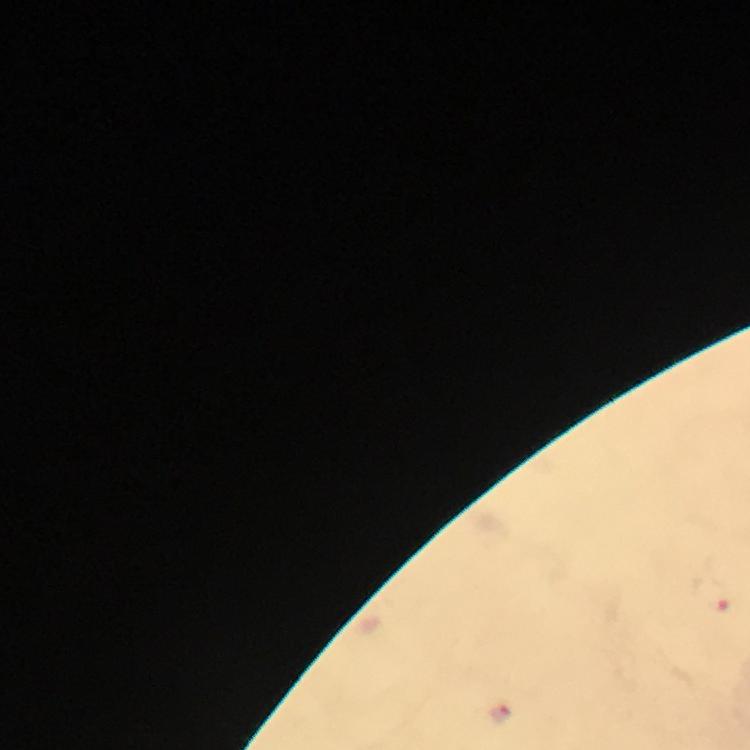

Approximate object centers, in pixels from the top-left corner.
Summary:
  - Malaria parasite locations: (x=724, y=607), (x=505, y=714)
  - Preparation: thick blood smear
  - Cropped from: a single field of view
  - Stain: Giemsa
  - Magnification: 100x
  - Image size: 750×750 pixels
  - Capture: smartphone camera through the microscope
  - Context: from a diagnostic examination for malaria
  - Immersion oil: applied